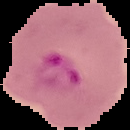

{
  "result": "Plasmodium parasites identified",
  "image_size": "130×130 pixels",
  "preparation": "thin blood film",
  "image_type": "segmented cell region with the area outside set to black"
}